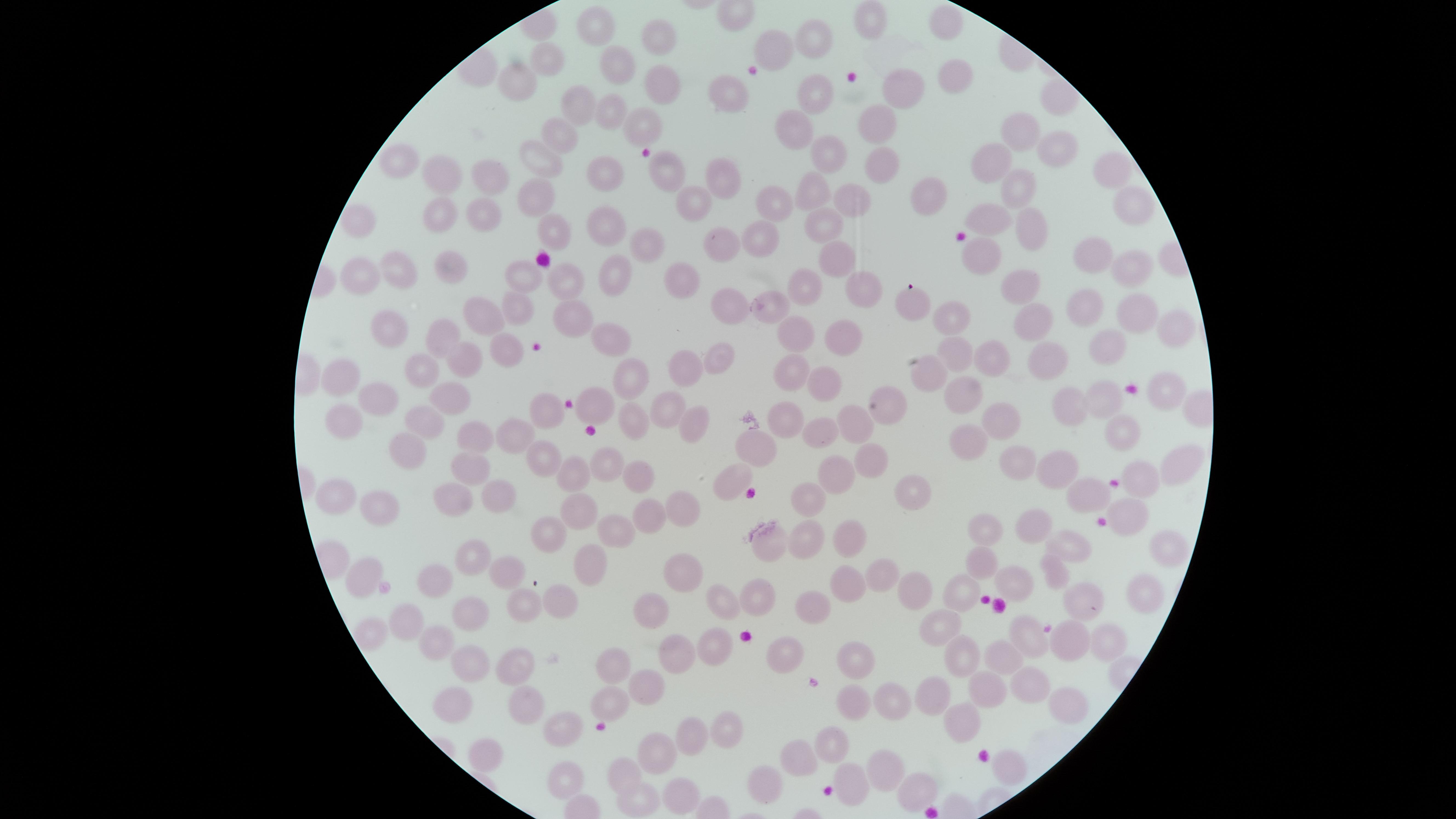
capture = smartphone photograph through the microscope eyepiece
uninfected red blood cells = approximate marker points as [x, y] in pixels: [870, 23], [947, 24], [594, 26], [815, 32], [778, 40], [661, 41], [548, 56], [624, 65], [955, 79], [520, 81], [665, 86], [904, 88], [811, 90], [725, 92], [574, 104], [603, 114], [639, 123], [880, 127], [790, 129], [1016, 132], [562, 133], [1054, 144], [405, 153], [822, 153], [992, 154], [552, 158], [885, 161], [611, 165], [1110, 167], [669, 170], [717, 174], [440, 175], [490, 176], [815, 185], [1017, 185], [929, 194], [536, 195], [853, 196], [694, 199], [773, 203], [1126, 204], [440, 209], [487, 209], [992, 218], [827, 222], [357, 224], [1032, 227], [557, 228], [598, 231], [757, 237], [649, 238], [716, 249], [1090, 249], [837, 254], [979, 255], [453, 266], [1122, 266], [612, 268], [397, 272], [566, 274], [524, 275], [681, 279], [360, 280], [809, 280], [863, 280], [1026, 281], [915, 302], [722, 305], [775, 305], [514, 308], [1081, 315], [1135, 315], [479, 317], [562, 319], [952, 319], [1034, 323], [1174, 328], [599, 330], [384, 332], [794, 333], [842, 333], [434, 336], [1109, 346], [952, 349], [505, 352], [987, 353], [723, 354], [1045, 355], [469, 356], [683, 361], [787, 364], [427, 370], [630, 375], [928, 376], [348, 378], [819, 380], [1159, 385], [973, 391], [452, 392], [1105, 395], [374, 398], [890, 401], [1072, 401], [669, 404], [596, 405], [539, 406], [344, 415], [997, 417], [420, 418], [784, 418], [857, 418], [630, 422], [695, 423], [814, 426], [1115, 429], [477, 439], [970, 439], [512, 440], [754, 444], [407, 449], [872, 457], [548, 459], [1028, 464], [612, 466], [470, 467], [1172, 467], [1059, 468], [840, 472], [577, 477], [732, 479], [633, 480], [1142, 482], [919, 487], [453, 489], [502, 491], [810, 494], [1088, 494], [341, 497], [385, 505], [682, 507], [1131, 507], [652, 512], [580, 518], [1032, 518], [984, 526], [617, 527], [550, 536], [806, 536], [765, 540], [848, 541], [1068, 545], [1157, 547], [468, 554], [593, 564], [987, 564], [508, 568], [684, 568], [367, 570], [1052, 571], [442, 577], [886, 577], [846, 582], [1021, 590], [1137, 592], [916, 595], [962, 595], [725, 599], [1084, 599], [757, 601], [523, 602], [557, 602], [659, 609], [810, 609], [409, 611], [474, 611], [935, 628], [1032, 637], [1067, 638], [429, 639], [1109, 642], [715, 645], [786, 648], [676, 651], [613, 658], [469, 660], [960, 660], [520, 662], [854, 662], [998, 662], [647, 677], [1032, 682], [987, 683], [450, 695], [937, 696], [894, 697], [846, 699], [524, 701], [612, 701], [1064, 704], [960, 722], [722, 731], [687, 735], [833, 738], [481, 753], [797, 754], [652, 759], [1004, 766], [627, 767], [879, 768], [765, 778], [562, 779], [858, 785], [679, 789], [911, 792], [636, 798]
stain = Giemsa
image size = 1456×819 pixels
visible region = circular
presence = no malaria parasites identified
preparation = thin blood smear
field of view = single